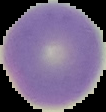 Malaria status: uninfected. Cell region segmented out of the field of view; the surrounding area is masked to black. From a thin blood film. Image is 106×112 pixels.